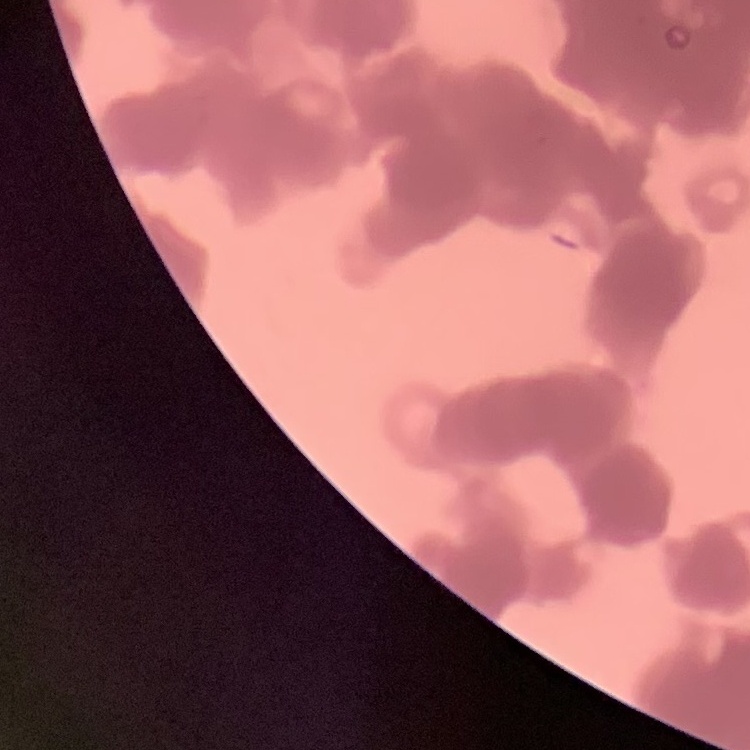
{
  "erythrocyte_morphology": "rouleaux formation",
  "stain": "Field's or Giemsa",
  "image_type": "one tile cut from a larger photomicrograph",
  "preparation": "thin blood smear"
}